Assess the morphology of the erythrocytes.
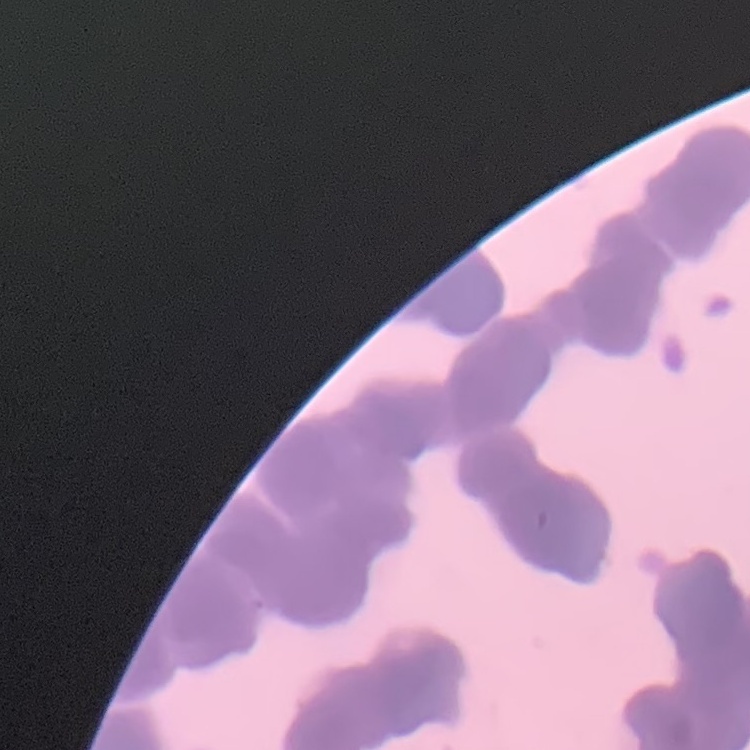

Rouleaux formation.

Thin blood smear. Stained with either Field's or Giemsa. Square crop of a larger photomicrograph.